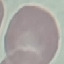

Summary:
  - Result: no malaria parasites detected
  - Stain: Giemsa
  - Preparation: thin blood smear
  - Capture: smartphone through the microscope eyepiece
  - Image type: cell patch, automatically extracted from a larger field of view and resized to 64 × 64 pixels